Assess the morphology of the erythrocytes.
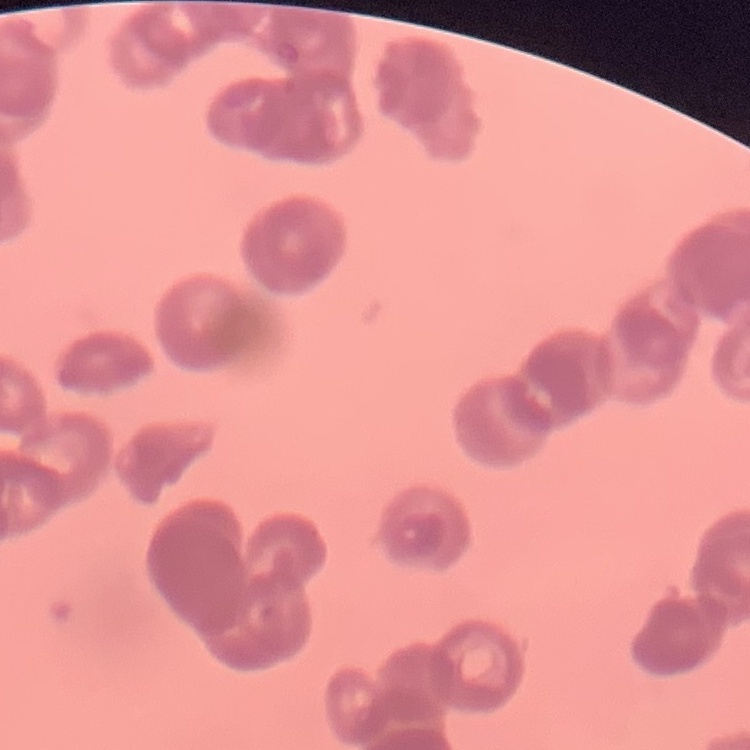

They show rouleaux formation.

{
  "stain": "Field's or Giemsa",
  "image_type": "one tile cut from a larger photomicrograph",
  "preparation": "thin blood smear"
}